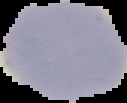

image size = 127×103 pixels
image type = segmented cell region on a black background
preparation = thin blood smear
result = no Plasmodium parasites detected